Locate every blood parasite and identify its species.
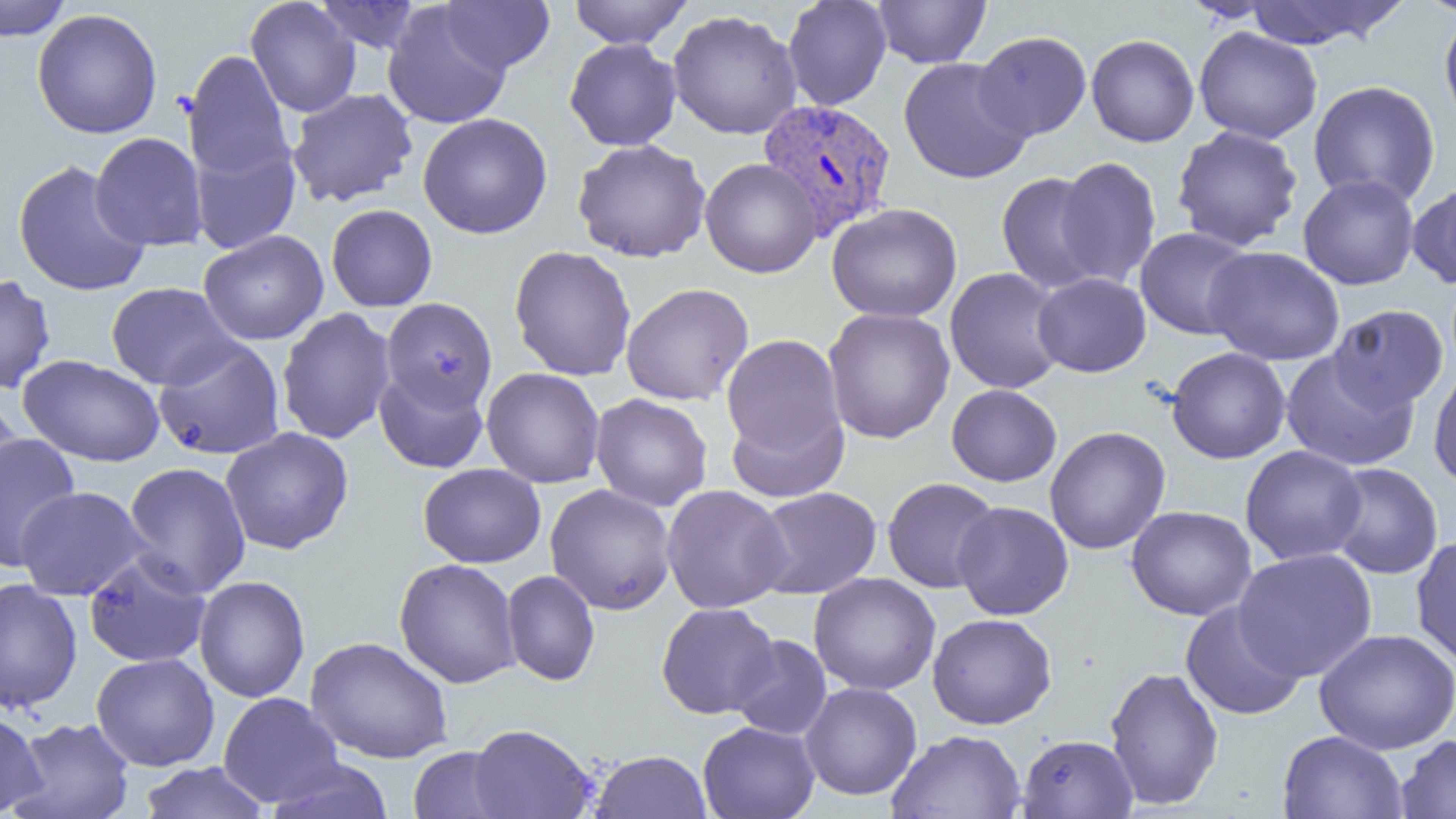

Approximate bounding boxes as (x1, y1, x2, y2) in pixels.
Plasmodium vivax-infected red blood cells: (757, 98, 897, 241).
No Plasmodium falciparum, Plasmodium ovale, Plasmodium malariae, Babesia divergens, or Trypanosoma brucei observed.

slide-level diagnosis = Plasmodium vivax
magnification = 1000x
field of view = single
modality = light microscopy
image size = 1456×819 pixels
uninfected red blood cell locations = approximate bounding boxes as (x1, y1, x2, y2) in pixels: (0, 0, 74, 41), (313, 0, 421, 54), (440, 0, 554, 74), (568, 0, 692, 49), (782, 0, 892, 110), (872, 0, 991, 68), (1416, 0, 1456, 17), (246, 1, 361, 117), (1242, 1, 1406, 49), (382, 3, 512, 130), (31, 8, 163, 139), (1439, 9, 1456, 133), (667, 10, 802, 139), (1194, 26, 1323, 144), (973, 31, 1092, 141), (1086, 34, 1199, 147), (564, 38, 682, 151), (183, 49, 294, 184), (898, 57, 1034, 184), (1308, 80, 1441, 207), (287, 87, 418, 208), (418, 112, 552, 239), (1171, 125, 1304, 252), (90, 132, 208, 252), (189, 136, 300, 254), (572, 139, 711, 262), (1054, 156, 1161, 289), (700, 158, 822, 278), (12, 160, 151, 297), (996, 172, 1108, 294), (1298, 174, 1419, 290), (1408, 179, 1456, 289), (826, 203, 963, 323), (326, 204, 437, 312), (1135, 227, 1255, 340), (198, 229, 329, 345), (509, 245, 636, 381), (1203, 246, 1345, 366), (945, 267, 1067, 394), (1032, 272, 1151, 377), (0, 274, 56, 395), (105, 282, 241, 390), (621, 283, 754, 406), (381, 297, 498, 413), (1328, 304, 1448, 411), (276, 307, 396, 445), (822, 307, 955, 444), (721, 333, 847, 470), (152, 338, 286, 460), (1166, 347, 1291, 464), (1280, 350, 1419, 471), (18, 354, 165, 466), (1428, 365, 1456, 490), (482, 367, 605, 488), (374, 368, 488, 474), (946, 384, 1062, 487), (590, 393, 712, 512), (0, 399, 23, 508), (725, 402, 848, 503), (1045, 425, 1171, 554), (220, 427, 354, 555), (0, 433, 81, 573), (1240, 445, 1368, 565), (122, 461, 251, 598), (1327, 462, 1443, 579), (418, 463, 546, 568), (882, 477, 1001, 593), (545, 483, 677, 615), (661, 484, 792, 613), (15, 486, 149, 600), (752, 486, 882, 599), (952, 501, 1073, 620), (1125, 505, 1257, 621), (1410, 534, 1456, 668), (1232, 548, 1377, 682), (83, 551, 213, 669), (394, 558, 521, 688), (501, 570, 600, 686), (809, 572, 941, 695), (194, 575, 310, 703), (0, 579, 83, 713), (1180, 601, 1307, 721), (656, 602, 779, 719), (927, 613, 1057, 729), (1314, 628, 1455, 754), (729, 634, 833, 740), (305, 636, 453, 764), (91, 652, 220, 771), (1104, 665, 1224, 811), (799, 682, 922, 800), (218, 692, 345, 808), (0, 711, 46, 817), (9, 716, 135, 819), (698, 721, 820, 819), (467, 723, 598, 818), (888, 729, 1026, 819), (1278, 731, 1408, 819), (1018, 734, 1138, 818), (1396, 734, 1456, 819), (408, 746, 514, 819), (589, 749, 711, 819), (265, 759, 394, 819), (137, 761, 271, 818)
preparation = thin blood smear